Assess this cell for malaria.
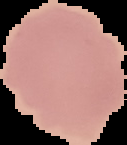

Uninfected.

Summary:
  - Image type: segmented cell region on a black background
  - Image size: 127×145 pixels
  - Preparation: thin blood film